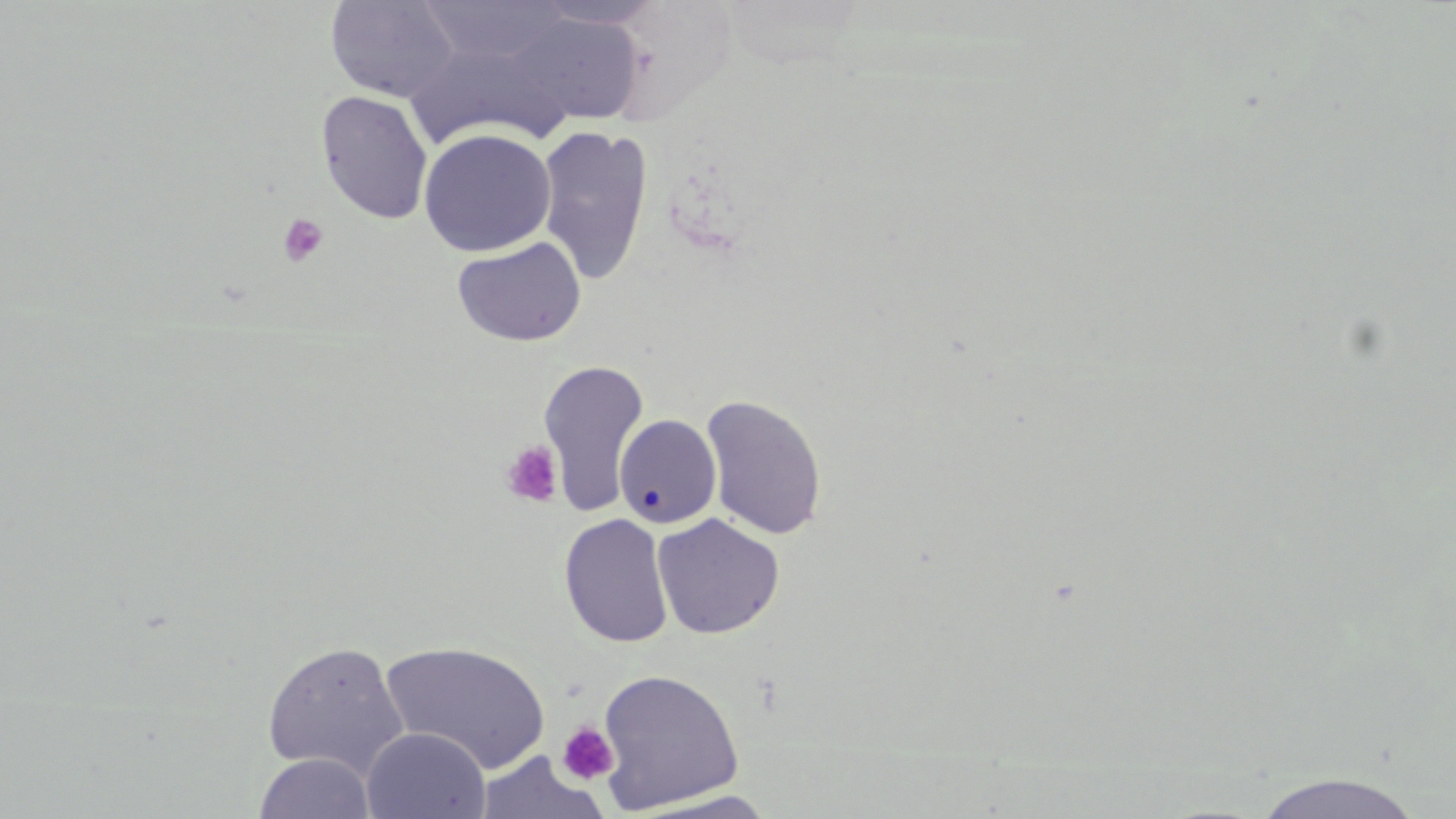 Approximate bounding boxes as (x1, y1, x2, y2) in pixels. Platelet locations: (278, 213, 329, 267), (500, 440, 563, 508), (557, 722, 618, 785). Uninfected red blood cell locations: (416, 0, 574, 66), (325, 1, 462, 103), (526, 1, 668, 30), (502, 12, 644, 128), (315, 90, 434, 224), (534, 123, 655, 285), (418, 128, 556, 256), (452, 236, 587, 347), (538, 358, 650, 515), (700, 393, 828, 540), (614, 414, 723, 528), (558, 513, 674, 648), (652, 513, 785, 639), (262, 640, 410, 778), (380, 640, 552, 772), (595, 667, 745, 814), (361, 728, 491, 819), (473, 751, 609, 819), (253, 752, 377, 819), (1251, 772, 1426, 819), (624, 790, 783, 818). Slide-level diagnosis: negative for blood parasites. Single field of view. Image is 1456×819 pixels. Captured at 1000x magnification. Thin blood smear. Light microscopy. May-Grünwald-Giemsa-stained preparation.